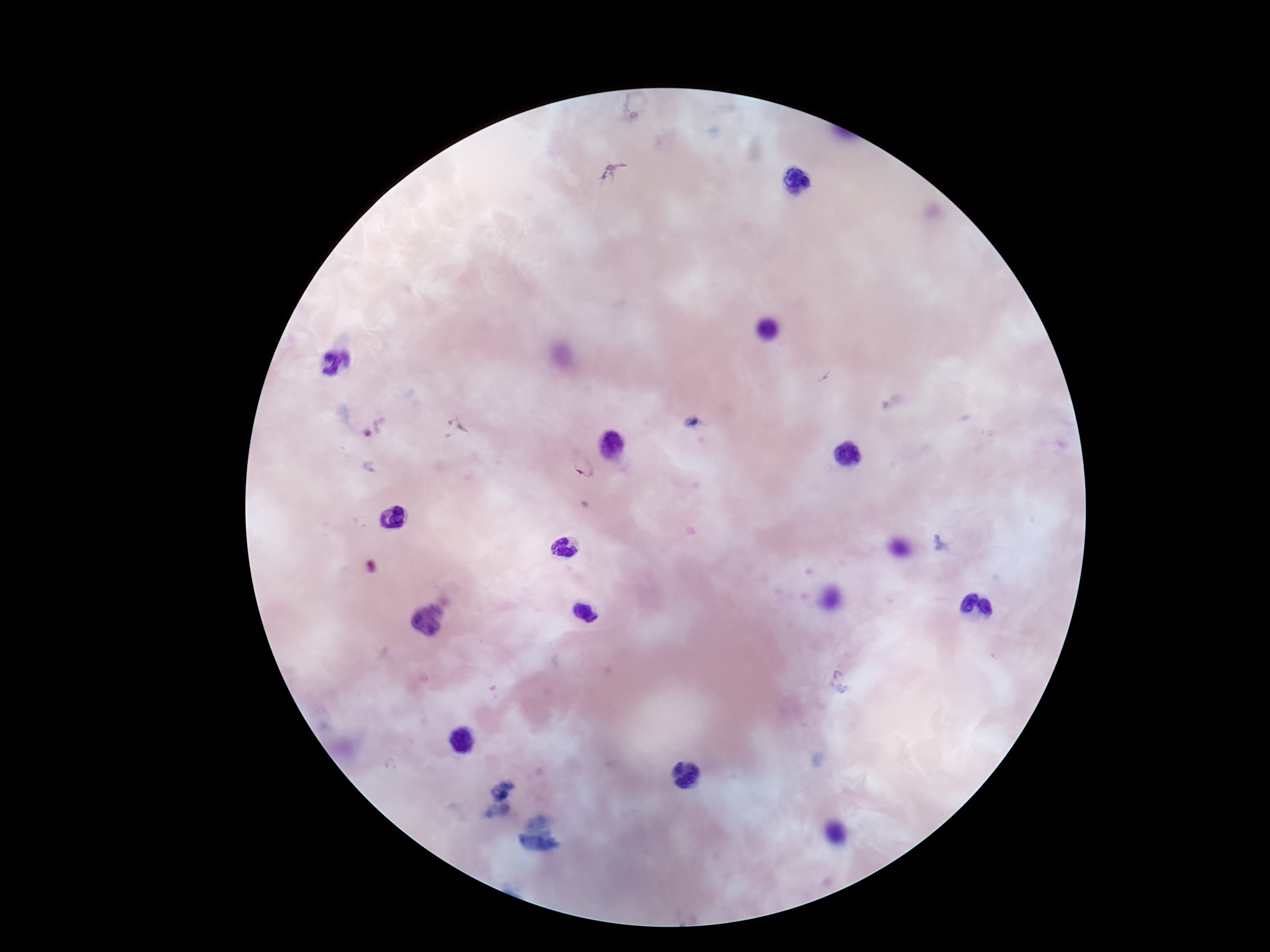

Approximate centers as {x, y} in pixels.
Summary:
  - Plasmodium parasite locations: {582, 472}
  - Preparation: thick blood film
  - Field of view: single
  - Patient malaria status: infected
  - Magnification: 100x
  - Stain: Giemsa
  - Image size: 1270×952 pixels
  - Capture: smartphone camera through the microscope eyepiece